Classify this cell by malaria status.
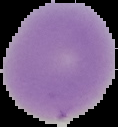

It is uninfected.

Summary:
  - Preparation: thin blood film
  - Image size: 118×127 pixels
  - Image type: cell region segmented out of the field of view; surrounding area masked to black